Outline each Plasmodium falciparum-infected red blood cell.
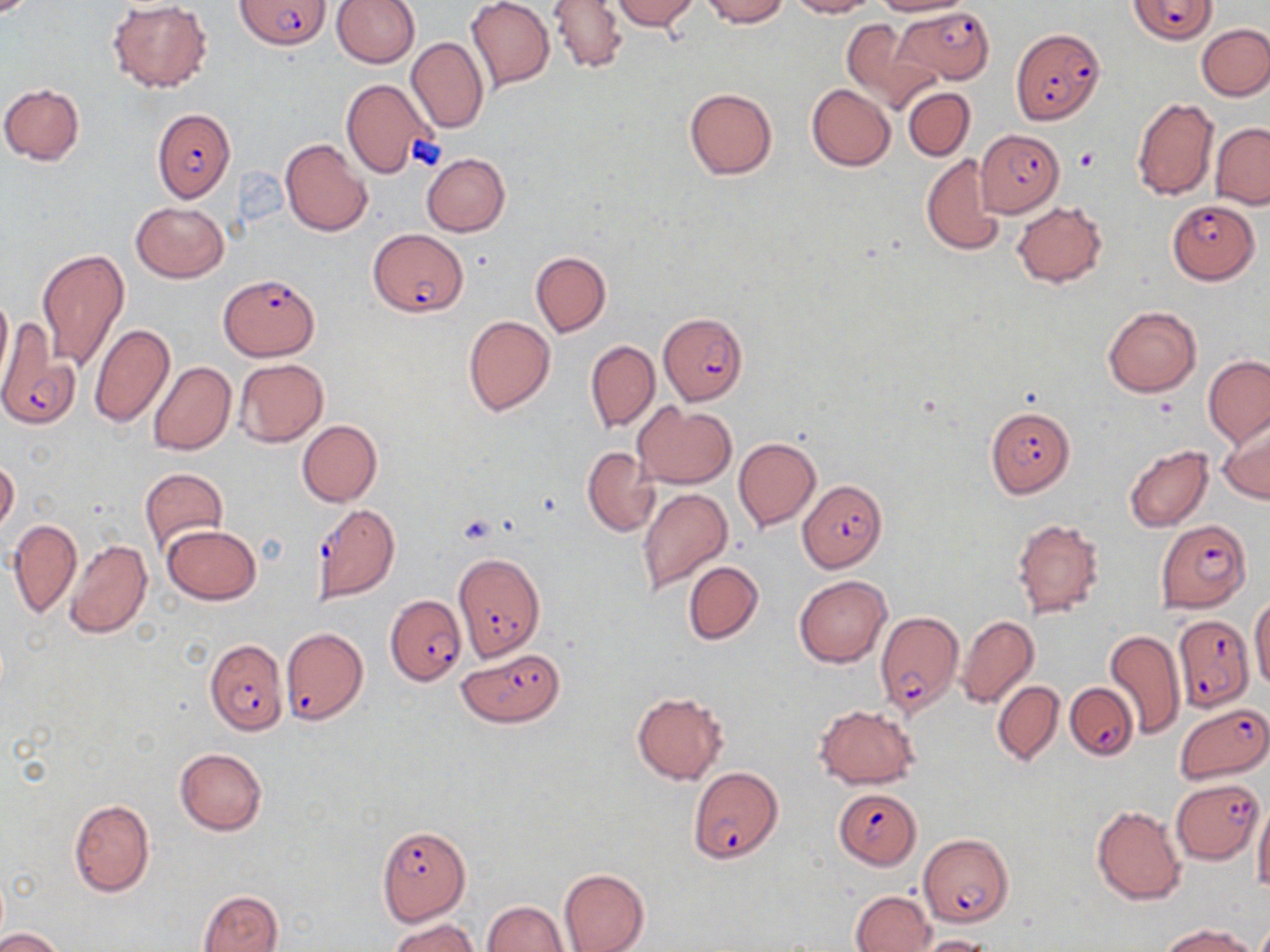
Approximate bounding boxes as (x1, y1, x2, y2) in pixels.
Plasmodium falciparum-infected red blood cells: (1128, 0, 1217, 43), (236, 1, 330, 50), (896, 7, 995, 84), (1011, 27, 1104, 124), (151, 109, 235, 202), (976, 129, 1063, 218), (1167, 199, 1258, 284), (368, 228, 468, 318), (221, 273, 320, 362), (658, 311, 748, 406), (0, 318, 78, 430), (986, 405, 1076, 498), (798, 480, 887, 571), (310, 504, 400, 603), (1154, 519, 1249, 611), (452, 551, 545, 662), (386, 596, 465, 686), (875, 611, 964, 715), (1172, 616, 1254, 711), (281, 626, 368, 726), (203, 638, 289, 736), (457, 648, 564, 728), (1067, 683, 1137, 760), (1177, 703, 1269, 782), (687, 768, 782, 863), (1171, 777, 1263, 863), (834, 789, 919, 869), (376, 825, 470, 925), (920, 832, 1014, 927).

Uninfected red blood cell locations: (330, 0, 420, 67), (466, 0, 555, 90), (609, 0, 700, 30), (700, 0, 787, 26), (786, 0, 876, 17), (872, 0, 970, 16), (107, 1, 211, 91), (548, 1, 628, 73), (839, 18, 936, 114), (1197, 23, 1270, 99), (407, 37, 488, 134), (341, 79, 432, 178), (0, 82, 86, 165), (807, 84, 896, 170), (685, 87, 777, 180), (902, 87, 975, 159), (1131, 98, 1219, 201), (1210, 123, 1270, 209), (280, 140, 372, 236), (421, 152, 510, 236), (922, 154, 1005, 258), (130, 200, 228, 283), (1012, 201, 1107, 287), (36, 247, 131, 372), (530, 251, 610, 337), (0, 289, 12, 383), (1103, 306, 1202, 397), (462, 315, 555, 416), (89, 323, 175, 427), (586, 340, 660, 432), (1203, 357, 1270, 446), (234, 359, 328, 446), (148, 361, 237, 456), (632, 402, 736, 488), (1219, 419, 1270, 503), (297, 420, 381, 506), (734, 437, 820, 531), (1124, 445, 1212, 533), (582, 448, 660, 536), (0, 456, 20, 536), (138, 467, 228, 554), (637, 488, 733, 594), (8, 518, 83, 619), (1011, 518, 1105, 618), (161, 525, 261, 605), (63, 540, 152, 640), (684, 561, 763, 644), (794, 575, 891, 667), (1249, 596, 1270, 694), (957, 616, 1038, 710), (1105, 629, 1186, 739), (992, 681, 1063, 766), (631, 690, 729, 785), (814, 704, 921, 788), (175, 747, 267, 834), (1252, 798, 1270, 894), (69, 799, 155, 897), (1091, 805, 1186, 905), (560, 868, 650, 952), (199, 889, 283, 952), (850, 890, 935, 951), (481, 901, 569, 952), (388, 918, 482, 952), (1160, 923, 1259, 952), (0, 928, 66, 952), (912, 935, 997, 952). Platelet locations: (1073, 148, 1100, 172), (457, 513, 498, 543). Slide-level diagnosis: Plasmodium falciparum. Image is 1270×952 pixels. One field of a larger specimen. Thin blood film. Optical microscopy. May-Grünwald-Giemsa stain. Captured at 1000x magnification.